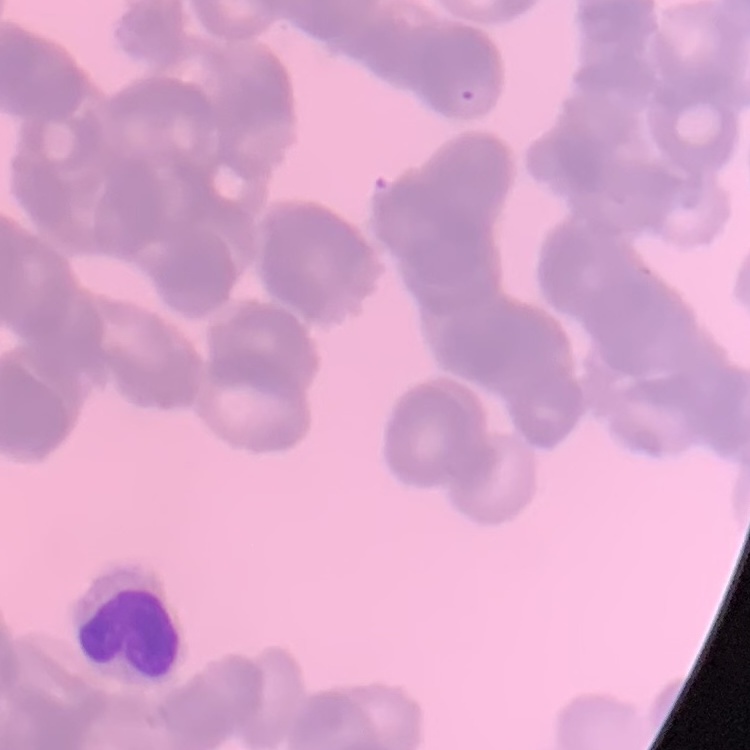
red_blood_cell_morphology: rouleaux formation
image_type: one tile cut from a larger photomicrograph
stain: Field's or Giemsa
preparation: thin blood film